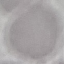
result = no malaria parasites detected
image type = cell patch, automatically extracted from a larger field of view and resized to 64 × 64 pixels
preparation = thin smear
capture = smartphone through the microscope eyepiece
stain = Giemsa